Locate platelets.
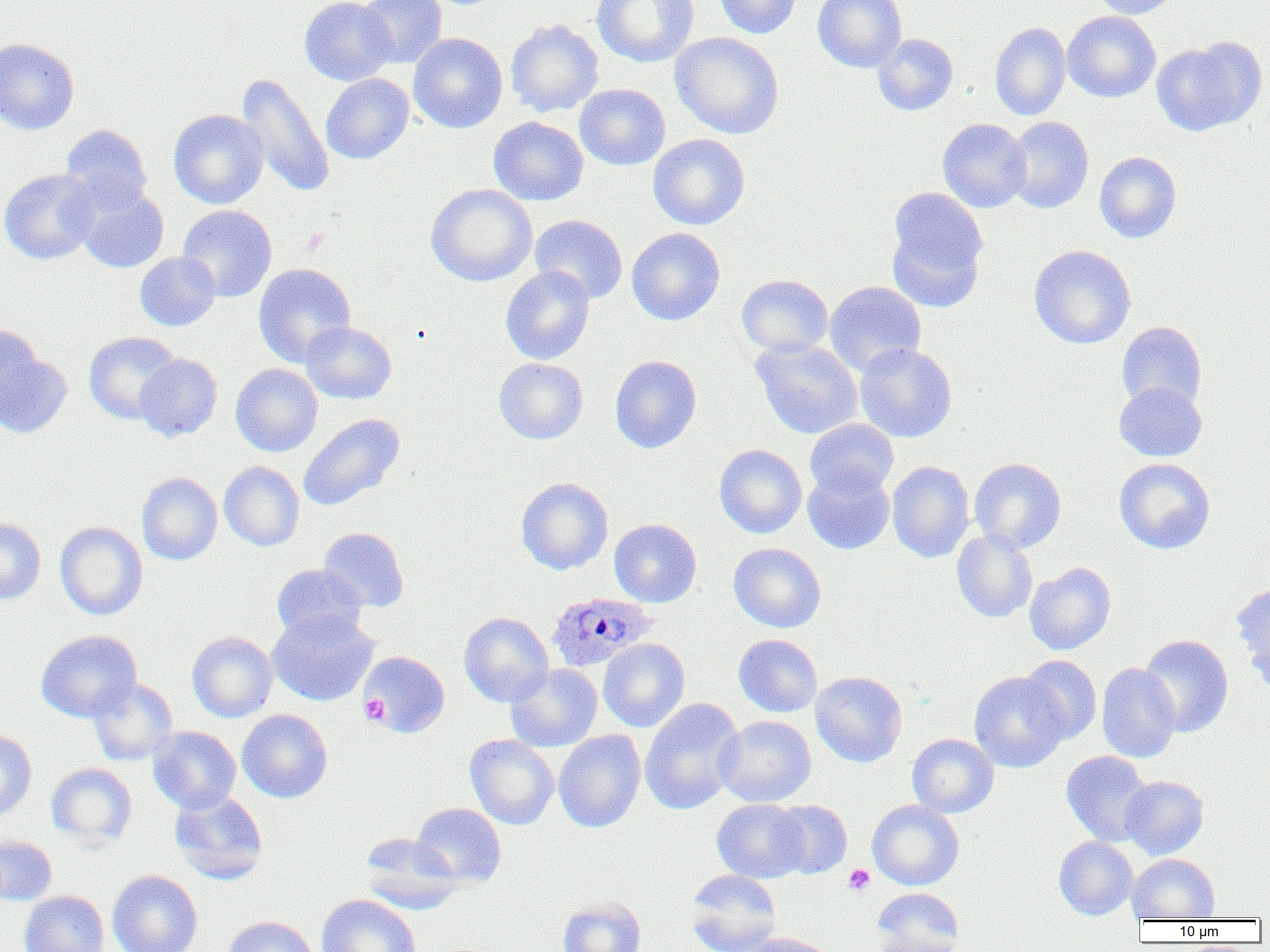

Approximate bounding boxes as (x1, y1, x2, y2) in pixels.
Platelets: (300, 229, 330, 256), (359, 694, 390, 725), (843, 864, 875, 896).

slide-level diagnosis = Plasmodium ovale
modality = light microscopy
magnification = 1000x
uninfected red blood cell locations = approximate bounding boxes as (x1, y1, x2, y2) in pixels: (299, 0, 397, 86), (358, 0, 447, 68), (592, 0, 699, 67), (714, 0, 802, 38), (813, 0, 907, 72), (1089, 0, 1181, 19), (1062, 11, 1161, 102), (505, 19, 603, 117), (989, 22, 1071, 120), (671, 31, 784, 139), (408, 33, 507, 133), (872, 33, 959, 115), (1152, 37, 1265, 136), (0, 38, 80, 135), (236, 72, 335, 198), (321, 73, 414, 164), (574, 83, 670, 170), (168, 109, 268, 209), (488, 116, 589, 205), (1006, 116, 1094, 213), (937, 118, 1031, 212), (60, 124, 152, 211), (648, 134, 750, 230), (1094, 151, 1181, 243), (0, 169, 100, 264), (76, 184, 169, 273), (426, 184, 537, 287), (886, 189, 988, 311), (177, 205, 277, 302), (529, 214, 627, 304), (626, 227, 725, 325), (1028, 245, 1136, 349), (135, 252, 221, 331), (253, 263, 356, 367), (501, 266, 595, 365), (737, 274, 833, 357), (824, 280, 926, 376), (300, 321, 397, 404), (1116, 321, 1207, 411), (0, 323, 43, 417), (84, 331, 182, 424), (751, 338, 863, 439), (854, 343, 957, 442), (0, 350, 71, 439), (135, 353, 223, 442), (610, 355, 701, 453), (494, 358, 588, 444), (230, 363, 323, 456), (1113, 381, 1206, 461), (298, 413, 405, 511), (805, 418, 899, 497), (714, 444, 807, 538), (969, 457, 1066, 552), (1114, 458, 1215, 554), (218, 461, 305, 551), (887, 461, 975, 563), (803, 465, 895, 554), (136, 472, 222, 565), (516, 477, 613, 575), (0, 517, 46, 605), (609, 518, 702, 607), (55, 522, 148, 620), (319, 527, 409, 612), (952, 529, 1038, 623), (728, 542, 826, 632), (1024, 562, 1116, 655), (271, 563, 368, 642), (1233, 583, 1270, 688), (267, 610, 377, 706), (458, 612, 554, 707), (36, 630, 141, 722), (187, 631, 278, 722), (734, 634, 822, 717), (1138, 634, 1233, 737), (598, 638, 690, 732), (358, 651, 450, 737), (1018, 655, 1102, 744), (505, 663, 602, 752), (1096, 663, 1182, 762), (810, 671, 908, 767), (969, 671, 1068, 772), (88, 678, 178, 766), (639, 698, 745, 815), (237, 709, 333, 803), (715, 715, 816, 807), (148, 726, 241, 813), (0, 730, 36, 822), (553, 730, 646, 832), (907, 733, 998, 818), (464, 734, 559, 829), (1061, 751, 1154, 847), (46, 762, 137, 847), (1120, 776, 1208, 860), (170, 790, 268, 884), (712, 798, 808, 882), (702, 799, 792, 951), (770, 800, 852, 878), (867, 800, 964, 890), (411, 802, 507, 888), (359, 833, 463, 913), (0, 834, 57, 906), (1054, 836, 1137, 919), (1127, 853, 1220, 921), (685, 869, 782, 952), (107, 870, 203, 952), (871, 888, 963, 952), (19, 890, 109, 952), (316, 893, 421, 952), (558, 897, 645, 952), (221, 915, 317, 952), (740, 932, 836, 952)
preparation = thin blood smear
image size = 1270×952 pixels
field of view = single
Plasmodium ovale-infected red blood cell locations = approximate bounding boxes as (x1, y1, x2, y2) in pixels: (547, 591, 657, 672)